Classify this cell by malaria status.
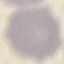
It is uninfected.

stain: Giemsa
capture: smartphone camera at the microscope eyepiece
preparation: thin smear
image_type: cell patch, automatically extracted from a larger field of view and resized to 64 × 64 pixels